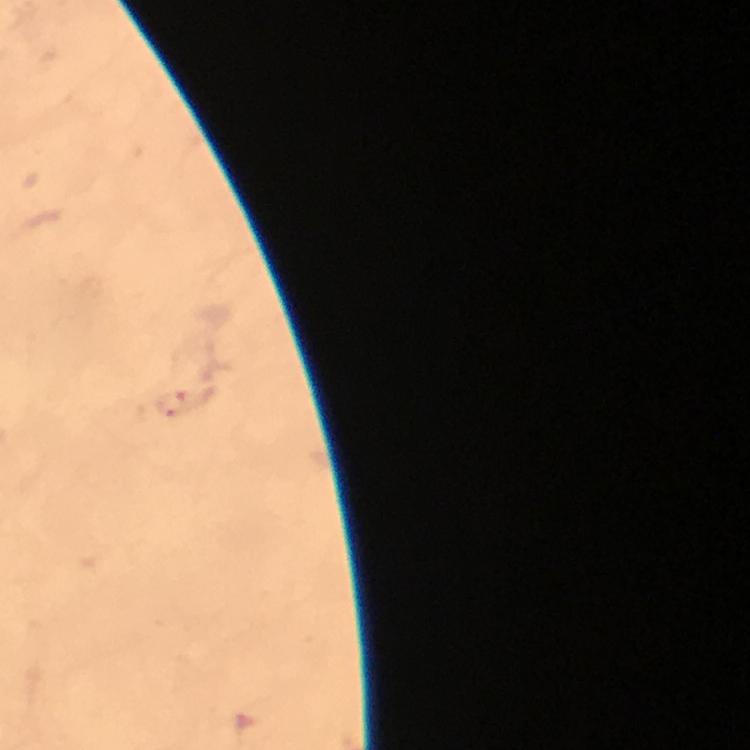

stain = Giemsa
context = from a diagnostic examination for malaria
preparation = thick blood film
immersion oil = applied
magnification = 100x
malaria parasite locations = approximate object centers, in pixels from the top-left corner: (x=170, y=404)
capture = smartphone photograph through a microscope
cropped from = a single field of view
image size = 750×750 pixels